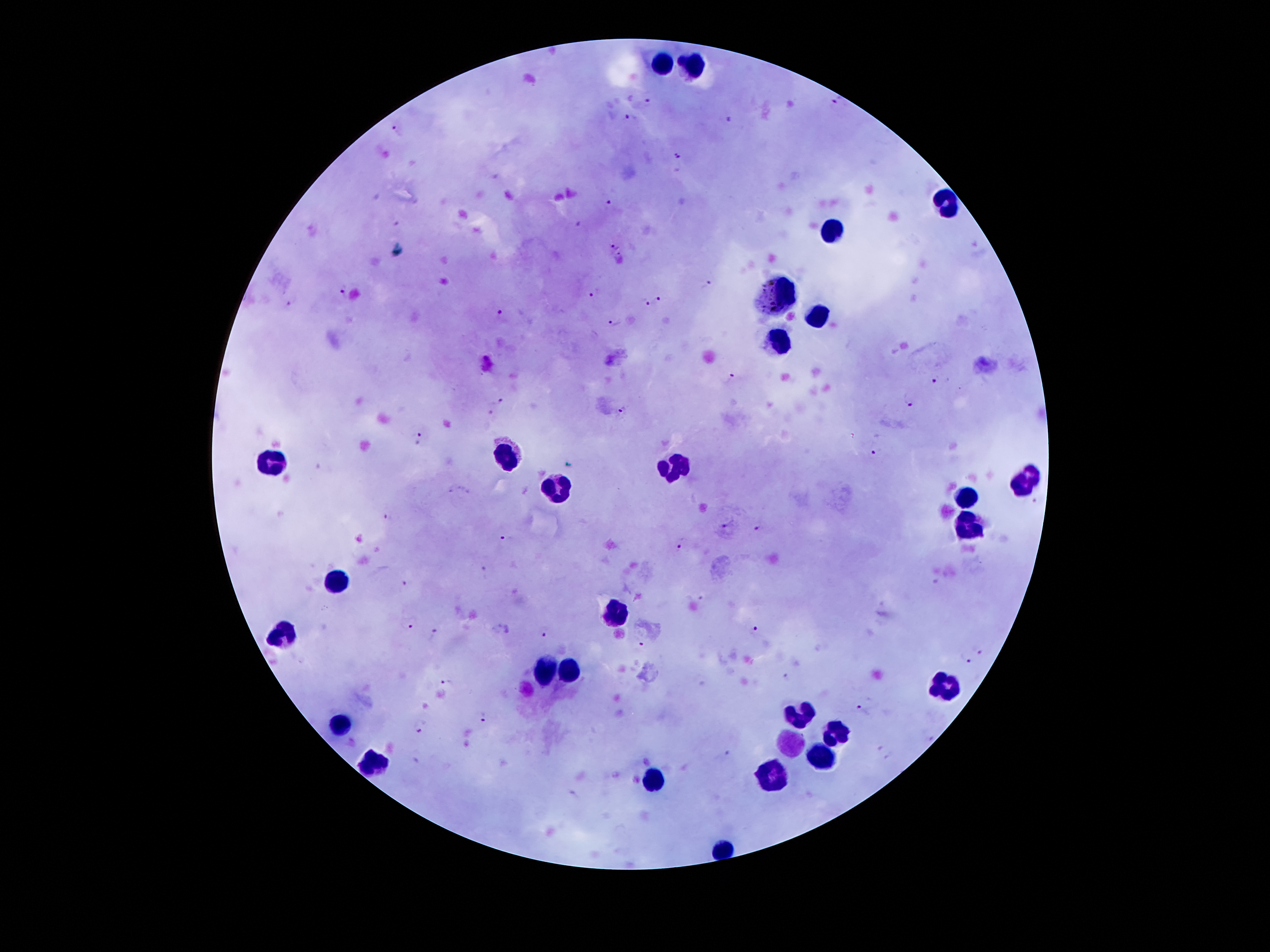

Approximate object centers, in pixels from the top-left corner.
Summary:
  - Plasmodium parasite locations: (x=838, y=100), (x=647, y=104), (x=629, y=120), (x=731, y=121), (x=396, y=131), (x=677, y=159), (x=608, y=206), (x=580, y=226), (x=614, y=246), (x=706, y=284), (x=343, y=290), (x=595, y=292), (x=657, y=300), (x=289, y=302), (x=645, y=303), (x=502, y=317), (x=614, y=321), (x=936, y=378), (x=734, y=380), (x=910, y=399), (x=502, y=400), (x=492, y=408), (x=624, y=414), (x=420, y=438), (x=873, y=453), (x=388, y=516), (x=728, y=523), (x=760, y=528), (x=505, y=537), (x=679, y=545), (x=483, y=572), (x=405, y=582), (x=411, y=626), (x=753, y=630), (x=544, y=631), (x=435, y=633), (x=643, y=641), (x=981, y=648), (x=967, y=661), (x=447, y=680), (x=860, y=711), (x=485, y=718), (x=420, y=726), (x=725, y=753), (x=883, y=755)
  - Leukocyte locations: (x=665, y=61), (x=697, y=61), (x=942, y=202), (x=828, y=231), (x=781, y=296), (x=819, y=313), (x=781, y=343), (x=509, y=458), (x=275, y=460), (x=678, y=467), (x=1026, y=481), (x=557, y=492), (x=966, y=495), (x=970, y=526), (x=335, y=582), (x=616, y=614), (x=284, y=630), (x=543, y=668), (x=565, y=672), (x=945, y=684), (x=804, y=714), (x=341, y=723), (x=833, y=733), (x=788, y=742), (x=825, y=758), (x=374, y=762), (x=776, y=777), (x=652, y=780), (x=723, y=850)
  - Preparation: thick blood smear
  - Magnification: 100x
  - Stain: Giemsa
  - Image size: 1270×952 pixels
  - Field of view: single
  - Patient malaria status: positive for Plasmodium falciparum
  - Capture: smartphone camera through the microscope eyepiece